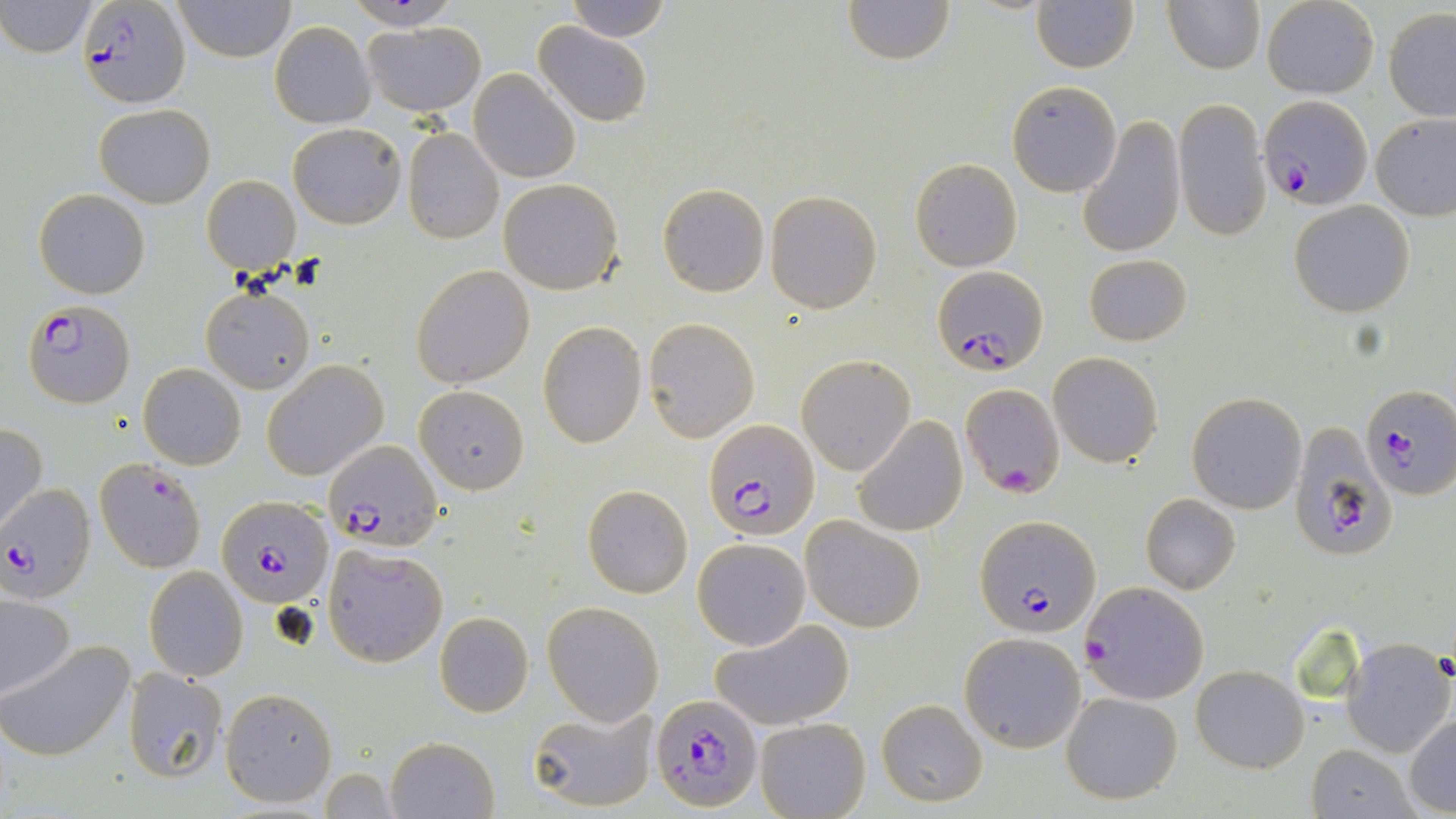
Summary:
  - Coordinate format: approximate bounding boxes as (x1,y1)-(x2,y2) corner pairs in pixels
  - Plasmodium falciparum-infected red blood cell locations: (79,3)-(189,105), (1259,94)-(1374,209), (931,266)-(1049,376), (23,301)-(135,409), (961,382)-(1066,500), (1360,383)-(1456,499), (702,418)-(823,540), (1287,423)-(1395,562), (323,439)-(444,551), (95,456)-(207,573), (0,485)-(96,603), (217,494)-(333,608), (976,515)-(1098,638), (1083,581)-(1208,704), (652,694)-(762,813)
  - Uninfected red blood cell locations: (172,0)-(295,62), (347,0)-(461,30), (564,0)-(673,42), (844,0)-(955,66), (1261,0)-(1379,98), (1,1)-(98,57), (1164,1)-(1265,75), (1032,2)-(1138,73), (1384,8)-(1456,122), (270,21)-(375,128), (364,21)-(486,115), (533,22)-(652,125), (470,69)-(578,184), (1007,80)-(1121,196), (1172,98)-(1270,242), (93,103)-(214,207), (1372,111)-(1456,220), (1078,115)-(1185,260), (288,122)-(405,229), (403,128)-(503,243), (910,157)-(1023,271), (201,175)-(300,275), (499,178)-(623,295), (657,183)-(770,297), (34,188)-(150,298), (765,190)-(882,313), (1288,199)-(1415,317), (1084,254)-(1192,346), (410,263)-(534,389), (201,287)-(315,394), (644,317)-(759,440), (538,321)-(647,447), (1048,352)-(1163,466), (797,355)-(915,474), (262,360)-(389,480), (139,363)-(244,469), (413,383)-(532,494), (1187,392)-(1306,514), (853,415)-(968,537), (0,422)-(48,531), (583,484)-(693,598), (1139,493)-(1240,594), (572,513)-(687,678), (800,516)-(923,632), (692,538)-(809,649), (322,543)-(448,667), (144,566)-(247,681), (0,594)-(76,700), (542,602)-(664,725), (434,612)-(534,717), (712,619)-(856,731), (960,632)-(1086,751), (1343,639)-(1455,757), (2,640)-(135,760), (1191,665)-(1309,772), (122,667)-(227,784), (220,687)-(338,807), (1060,690)-(1184,805), (877,700)-(987,807), (525,705)-(657,812), (1405,712)-(1456,815), (754,716)-(870,819), (385,735)-(500,819), (1306,745)-(1417,819), (317,769)-(397,817)
  - Slide-level diagnosis: Plasmodium falciparum
  - Preparation: thin blood film
  - Magnification: 1000x
  - Field of view: one of a larger specimen
  - Image size: 1456×819 pixels
  - Modality: optical microscopy
  - Stain: May-Grünwald-Giemsa